Point out each Plasmodium parasite.
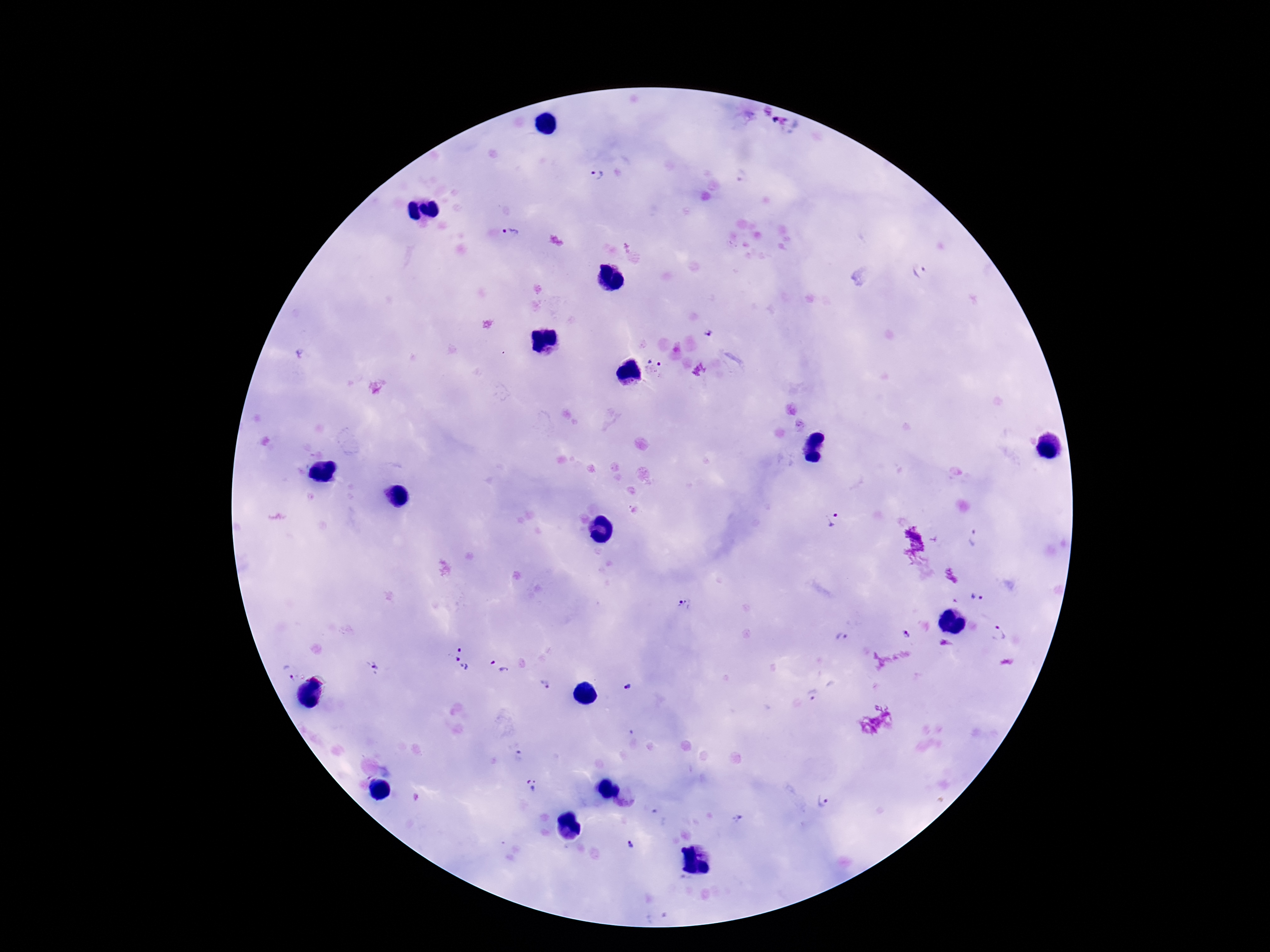

Approximate centers as [x, y] in pixels.
Plasmodium parasites: [592, 176], [742, 178], [512, 233], [920, 271], [708, 333], [300, 354], [654, 368], [832, 520], [976, 538], [978, 597], [685, 608], [998, 633], [907, 635], [843, 637], [462, 658], [500, 666], [374, 667], [288, 671], [546, 684], [625, 688], [813, 696], [518, 756], [533, 784], [823, 802], [738, 820], [630, 844].

stain = Giemsa
image size = 1270×952 pixels
magnification = 100x
field of view = one from this slide
preparation = thick blood smear
patient malaria status = positive
capture = smartphone camera through the microscope eyepiece